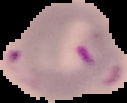
Image is 127×103 pixels. Segmented cell region on a black background. From a thin blood smear. Result: malaria parasites detected.